Outline each uninfected red blood cell.
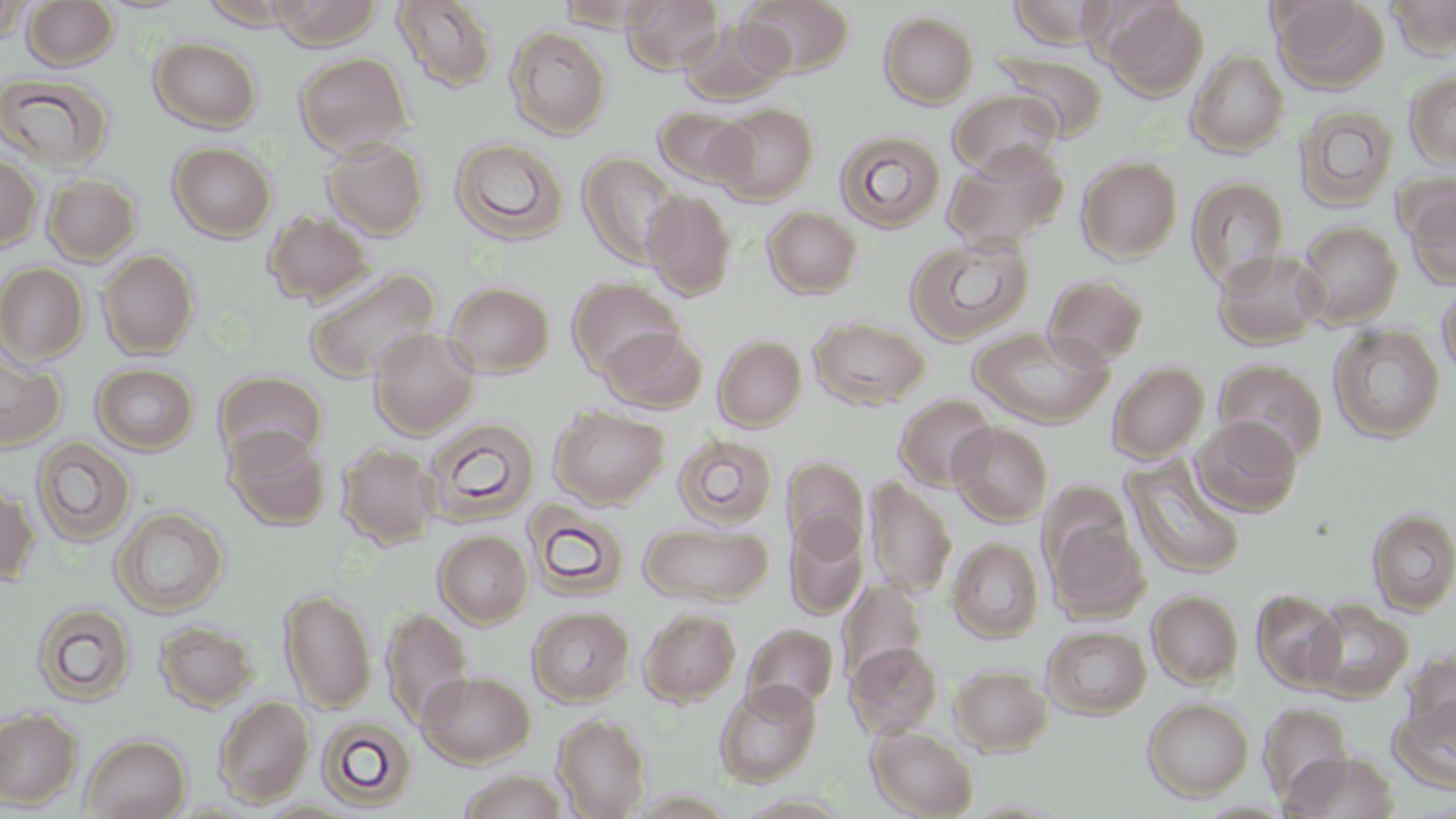
Approximate bounding boxes as (x1,y1)-(x2,y2) corner pairs in pixels.
Uninfected red blood cells: (22,0)-(118,69), (267,0)-(383,49), (622,0)-(724,74), (738,0)-(855,77), (1270,0)-(1390,93), (1386,0)-(1456,58), (392,1)-(498,92), (554,1)-(658,31), (1008,1)-(1114,48), (1101,1)-(1208,100), (0,3)-(29,45), (879,11)-(979,108), (679,17)-(792,106), (505,26)-(611,138), (149,37)-(262,132), (1187,50)-(1290,157), (293,51)-(414,156), (995,51)-(1109,141), (1404,70)-(1456,170), (0,71)-(113,171), (949,89)-(1062,178), (711,103)-(819,203), (1295,104)-(1399,212), (653,107)-(754,188), (834,130)-(946,232), (322,137)-(429,239), (450,137)-(569,246), (168,142)-(276,241), (943,143)-(1069,250), (578,151)-(685,267), (0,154)-(41,251), (1076,156)-(1182,262), (42,173)-(142,264), (1187,176)-(1289,288), (1402,182)-(1456,290), (643,190)-(737,299), (763,206)-(862,298), (264,209)-(373,306), (1295,220)-(1402,327), (905,234)-(1034,344), (98,249)-(199,358), (1212,249)-(1327,349), (0,263)-(89,364), (303,268)-(441,384), (1043,274)-(1149,367), (566,276)-(684,378), (444,281)-(555,376), (1437,281)-(1456,380), (809,316)-(929,409), (1329,325)-(1445,442), (967,326)-(1113,427), (600,327)-(708,413), (369,328)-(480,438), (714,335)-(806,430), (0,348)-(66,451), (1214,359)-(1328,463), (1107,361)-(1209,463), (92,363)-(198,454), (213,370)-(327,467), (894,394)-(998,490), (549,405)-(669,507), (1193,416)-(1303,516), (424,417)-(540,526), (949,422)-(1053,525), (226,428)-(331,531), (673,434)-(777,528), (31,437)-(136,547), (337,443)-(441,547), (1121,454)-(1247,580), (783,455)-(869,555), (863,478)-(957,597), (0,483)-(39,587), (524,501)-(630,600), (111,506)-(228,616), (1368,507)-(1456,615), (785,513)-(867,619), (1046,515)-(1149,620), (638,520)-(774,606), (434,530)-(532,626), (946,533)-(1149,637), (948,537)-(1044,642), (838,578)-(927,683), (279,588)-(377,712), (1251,589)-(1346,692), (1147,590)-(1244,688), (1305,599)-(1413,702), (32,602)-(136,705), (526,605)-(635,705), (381,607)-(474,729), (639,608)-(742,706), (154,620)-(257,711), (743,623)-(838,714), (1042,625)-(1152,718), (846,641)-(943,738), (950,664)-(1053,755), (417,669)-(535,767), (716,680)-(821,785), (1391,693)-(1456,793), (214,696)-(314,806), (1142,696)-(1253,800), (1259,703)-(1354,806), (0,707)-(82,809), (553,713)-(650,818), (316,716)-(417,812), (867,725)-(979,818), (81,733)-(190,819), (1284,752)-(1400,818).

slide-level diagnosis = no evidence of blood parasites
field of view = single
preparation = thin blood smear
stain = May-Grünwald-Giemsa
magnification = 1000x
modality = light microscopy
image size = 1456×819 pixels